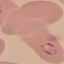

{
  "result": "malaria parasites identified",
  "image_type": "automatically extracted cell patch, resized to 64 × 64 pixels",
  "capture": "smartphone through the microscope eyepiece",
  "stain": "Giemsa",
  "preparation": "thin blood smear"
}